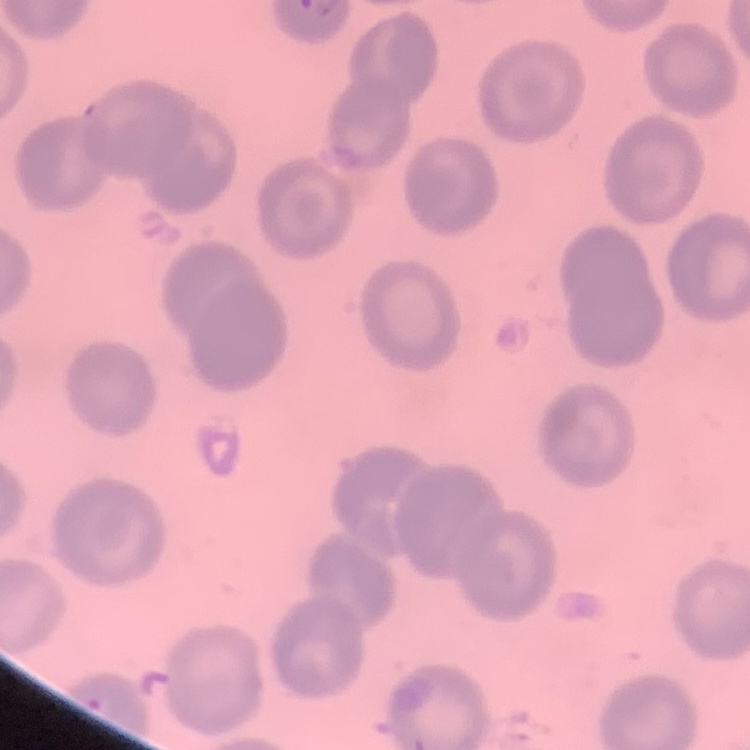
Summary:
  - Erythrocyte morphology: no rouleaux formation
  - Preparation: thin blood smear
  - Stain: Field's or Giemsa
  - Image type: square crop of a larger photomicrograph